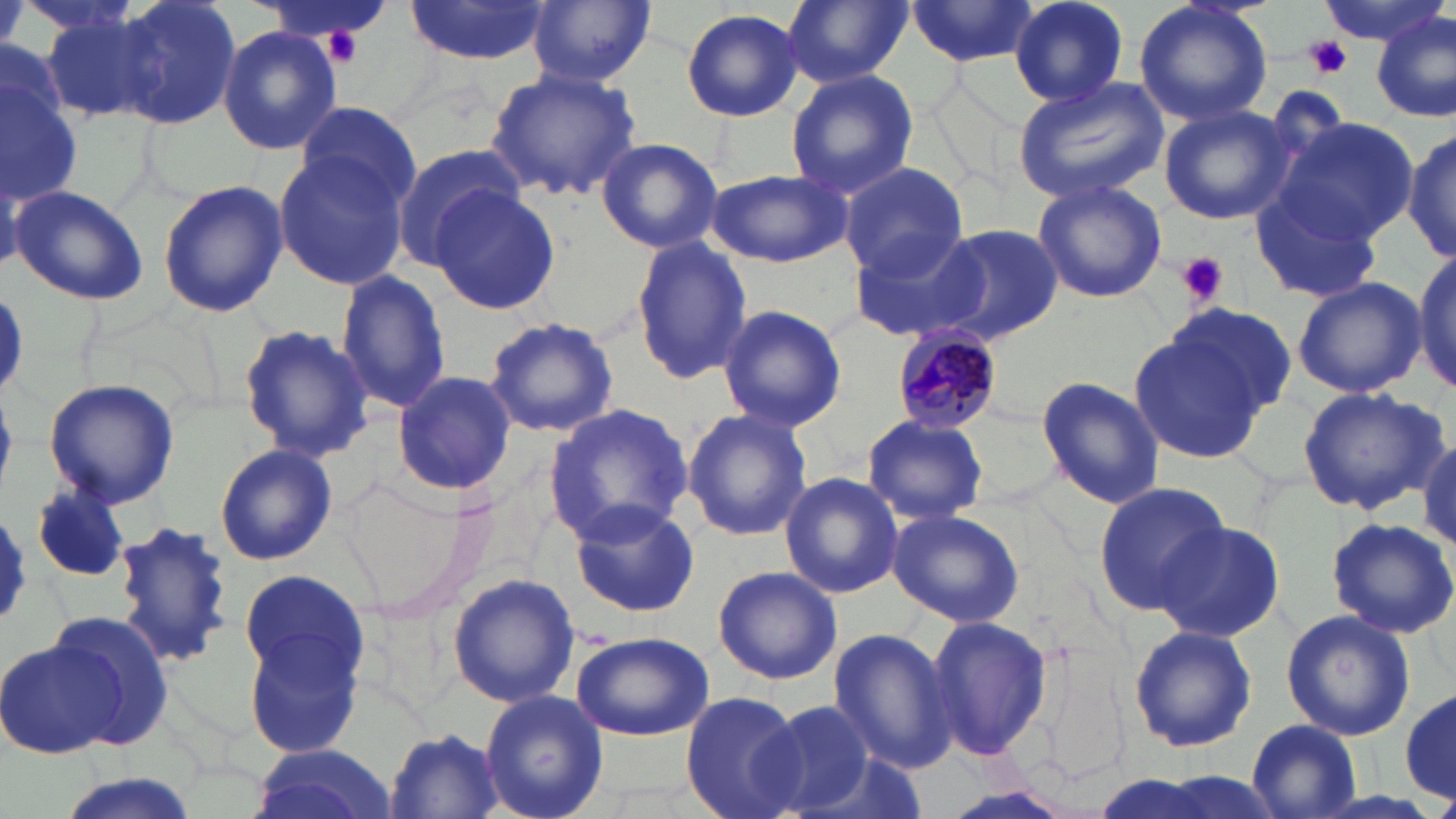

slide_level_diagnosis: Plasmodium malariae
preparation: thin blood film
stain: May-Grünwald-Giemsa
platelet_locations: 'approximate bounding boxes as [x1, y1, x2, y2] in pixels: [1307, 36, 1353, 78], [1176, 252, 1229, 306]'
modality: optical microscopy
uninfected_red_blood_cell_locations: 'approximate bounding boxes as [x1, y1, x2, y2] in pixels: [110, 0, 241, 128], [782, 0, 911, 87], [908, 0, 1040, 70], [1007, 0, 1130, 106], [1134, 0, 1275, 128], [1314, 0, 1445, 47], [405, 1, 550, 65], [526, 1, 656, 86], [36, 6, 161, 124], [680, 8, 806, 122], [1374, 11, 1454, 122], [217, 24, 342, 156], [0, 64, 85, 206], [484, 68, 641, 201], [785, 68, 916, 201], [1013, 76, 1170, 205], [1158, 104, 1294, 226], [294, 105, 423, 208], [1279, 117, 1421, 244], [1402, 126, 1456, 267], [596, 137, 724, 255], [391, 143, 529, 268], [272, 149, 413, 291], [838, 160, 967, 278], [706, 169, 850, 268], [156, 178, 289, 321], [1030, 178, 1167, 304], [430, 183, 562, 314], [1248, 183, 1387, 304], [8, 184, 149, 305], [930, 224, 1063, 345], [848, 227, 992, 342], [630, 236, 753, 382], [1406, 254, 1456, 392], [335, 269, 452, 418], [1292, 277, 1428, 398], [1166, 302, 1299, 418], [717, 303, 847, 432], [1126, 315, 1279, 464], [483, 316, 620, 438], [239, 324, 375, 466], [391, 371, 516, 497], [1034, 376, 1167, 508], [42, 378, 180, 509], [1297, 385, 1447, 516], [544, 404, 697, 543], [681, 407, 812, 542], [863, 416, 988, 526], [1415, 436, 1455, 550], [214, 444, 337, 565], [780, 472, 904, 598], [1091, 481, 1230, 615], [28, 482, 129, 584], [568, 498, 699, 618], [886, 505, 1025, 627], [1325, 516, 1456, 640], [112, 518, 231, 669], [1155, 521, 1285, 642], [711, 566, 842, 685], [234, 567, 375, 755], [448, 572, 580, 708], [45, 609, 178, 751], [1280, 609, 1417, 740], [923, 614, 1054, 764], [1127, 623, 1258, 754], [827, 627, 958, 773], [569, 629, 716, 741], [0, 637, 123, 760], [478, 688, 609, 819], [1399, 688, 1455, 806], [680, 691, 806, 819], [755, 701, 882, 817], [1247, 720, 1361, 816], [385, 728, 506, 817], [246, 744, 399, 819], [48, 774, 205, 819]'
image_size: 1456×819 pixels
plasmodium_malariae_infected_red_blood_cell_locations: 'approximate bounding boxes as [x1, y1, x2, y2] in pixels: [889, 326, 1004, 433]'
magnification: 1000x
field_of_view: single